Point out each Plasmodium parasite.
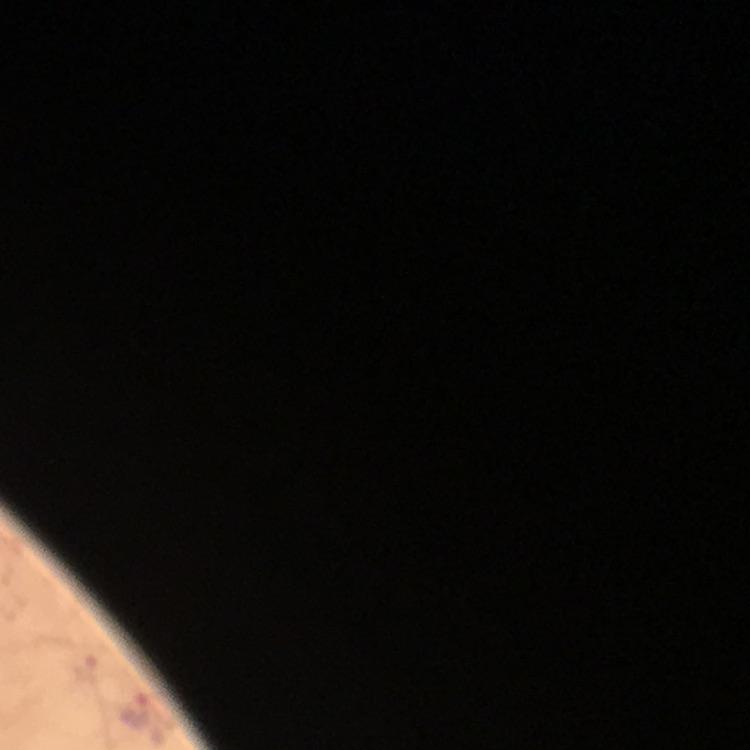

Approximate centers as (x, y) in pixels.
Plasmodium parasites: (87, 666), (136, 711).

Summary:
  - Preparation: thick smear
  - Cropped from: a single field of view
  - Capture: smartphone camera through the microscope
  - Stain: Giemsa
  - Magnification: 100x
  - Image size: 750×750 pixels
  - Immersion oil: used
  - Context: from a malaria diagnostic workup